Report the malaria status.
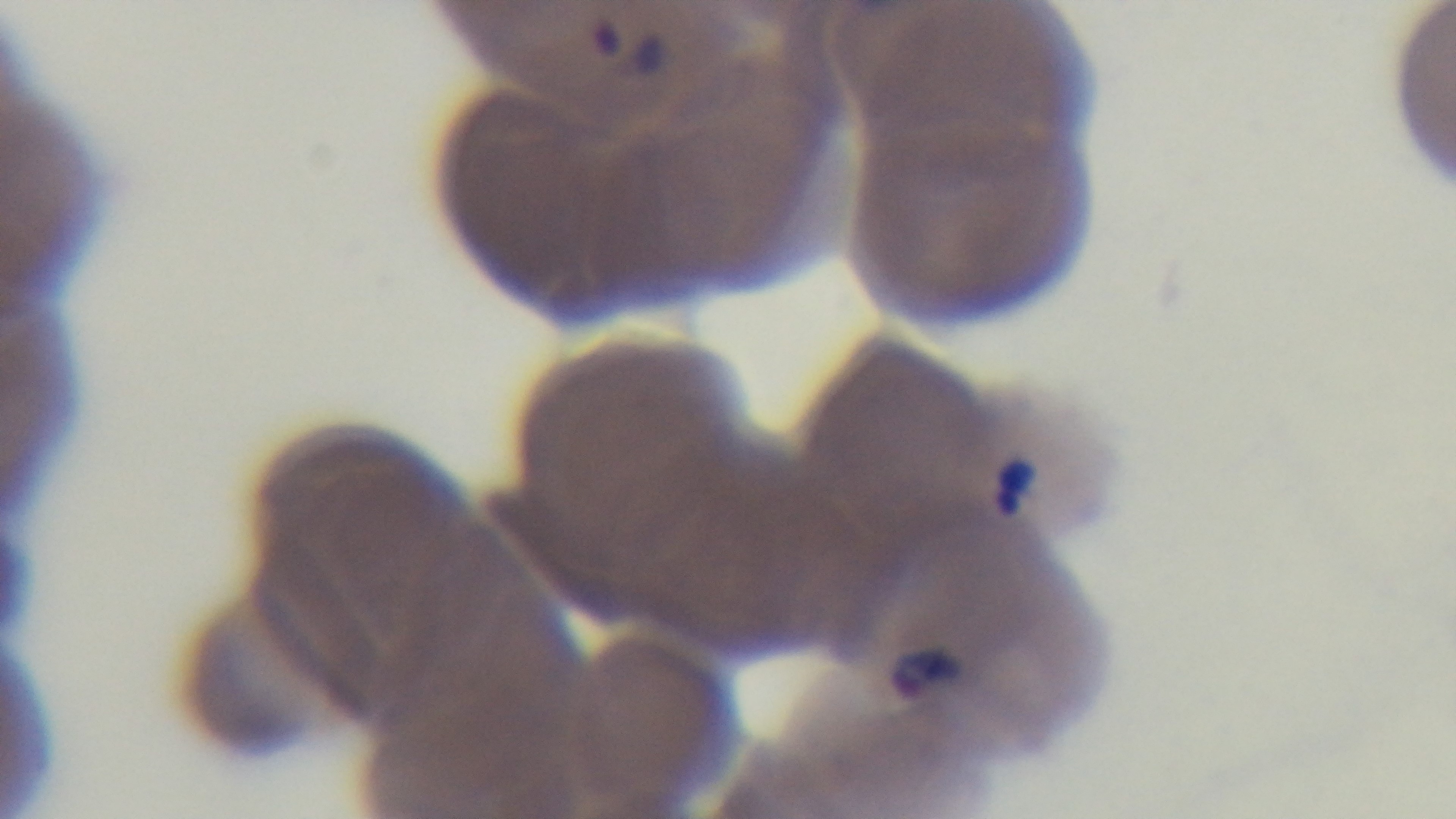
Positive.

Giemsa stain. 100x oil-immersion objective. Captured with a mounted 4K digital camera. Photomicrograph. Preparation: thin. Single field of view.